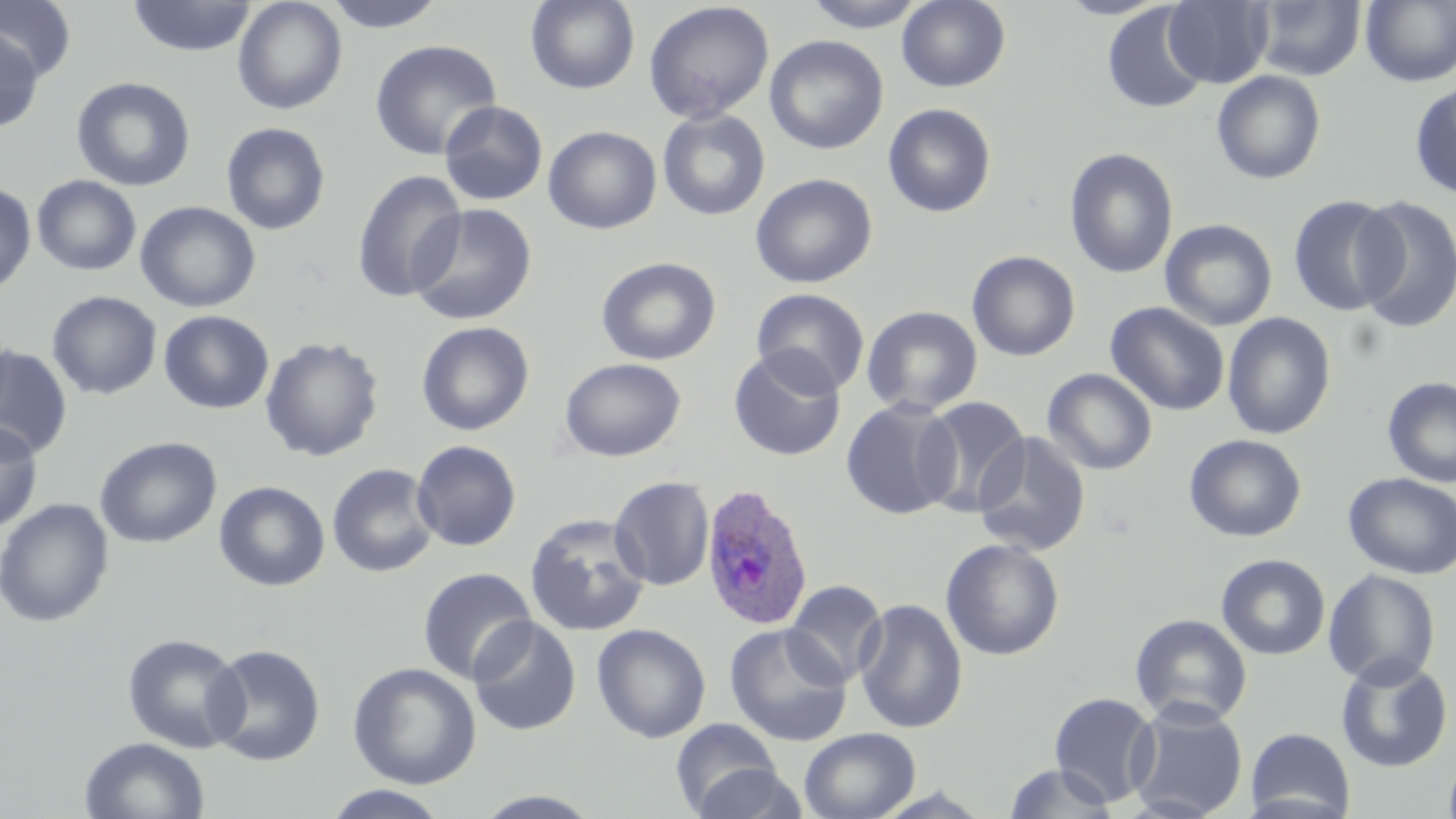
Summary:
  - Coordinate format: approximate bounding boxes as (x1,y1)-(x2,y2) corner pairs in pixels
  - Plasmodium ovale-infected red blood cell locations: (700,484)-(816,632)
  - Uninfected red blood cell locations: (127,0)-(256,57), (232,0)-(347,115), (322,0)-(448,32), (525,0)-(640,94), (896,0)-(1011,92), (1056,0)-(1172,20), (1164,0)-(1272,87), (1251,0)-(1366,80), (0,1)-(76,81), (803,1)-(928,32), (1361,1)-(1456,87), (643,2)-(774,123), (1102,3)-(1209,114), (0,29)-(43,132), (765,35)-(888,154), (370,40)-(501,160), (1211,70)-(1326,184), (71,77)-(195,192), (1410,82)-(1456,199), (439,100)-(548,205), (883,103)-(997,217), (657,109)-(771,221), (221,121)-(331,235), (543,125)-(662,234), (1064,147)-(1179,279), (351,170)-(467,303), (750,172)-(878,288), (32,175)-(141,275), (0,182)-(37,295), (1288,194)-(1403,317), (1352,195)-(1456,332), (136,201)-(261,313), (407,202)-(536,326), (1160,218)-(1277,331), (967,250)-(1080,362), (596,256)-(721,365), (751,288)-(870,397), (46,291)-(162,400), (1105,302)-(1230,415), (861,305)-(983,416), (159,310)-(273,414), (1222,312)-(1336,439), (416,321)-(535,436), (260,336)-(384,462), (0,345)-(73,460), (728,347)-(846,461), (559,357)-(686,462), (1042,368)-(1157,475), (1382,377)-(1456,487), (917,397)-(1029,516), (841,399)-(961,520), (0,420)-(43,532), (972,432)-(1091,556), (1184,434)-(1306,542), (95,436)-(222,548), (412,440)-(522,551), (327,463)-(439,578), (1343,472)-(1456,579), (609,476)-(714,591), (214,480)-(330,591), (0,498)-(114,627), (524,513)-(652,637), (940,537)-(1065,661), (1216,553)-(1330,660), (417,567)-(536,684), (1323,568)-(1441,688), (784,579)-(888,686), (854,598)-(968,735), (1130,614)-(1252,727), (467,616)-(582,736), (724,622)-(853,747), (591,623)-(711,743), (122,632)-(248,753), (203,643)-(326,766), (1336,654)-(1452,773), (348,662)-(482,789), (1049,692)-(1159,807), (1126,700)-(1249,819), (670,716)-(783,816), (799,727)-(921,819), (1246,727)-(1356,819), (79,736)-(210,819), (1443,753)-(1456,819), (689,762)-(808,818), (1004,763)-(1118,818), (322,785)-(450,819), (471,790)-(605,818)
  - Slide-level diagnosis: Plasmodium ovale
  - Image size: 1456×819 pixels
  - Preparation: thin blood film
  - Modality: light microscopy
  - Field of view: single
  - Magnification: 1000x
  - Stain: May-Grünwald-Giemsa